Report the malaria status of this cell.
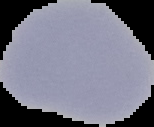

It is uninfected.

Summary:
  - Image type: cell region segmented out of the field of view; surrounding area masked to black
  - Image size: 154×127 pixels
  - Preparation: thin blood smear